Describe the morphology of the red blood cells.
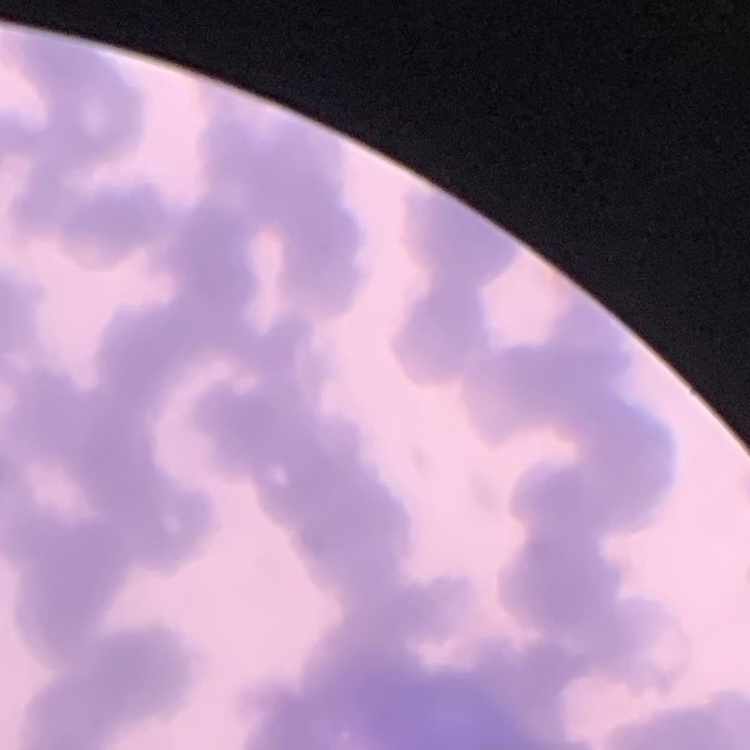
Rouleaux formation.

stain = Field's or Giemsa
preparation = thin peripheral smear
image type = square crop of a larger photomicrograph